Assess this cell for malaria.
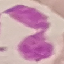
Uninfected.

Giemsa stain. Thin blood film. Acquired by smartphone through the microscope eyepiece. Automatically extracted cell patch, resized to 64 × 64 pixels.